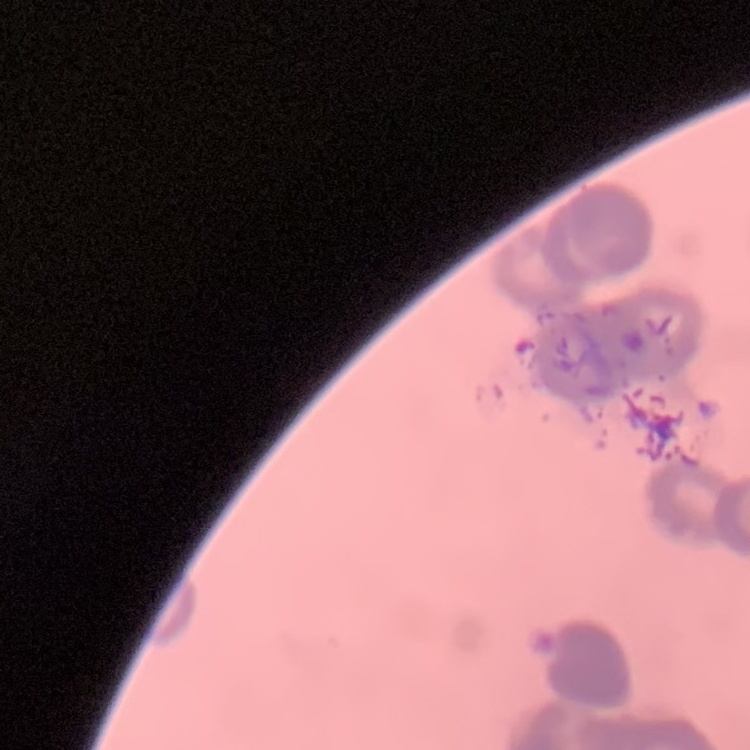

Summary:
  - Erythrocyte morphology: rouleaux formation
  - Preparation: thin peripheral smear
  - Stain: Field's or Giemsa
  - Image type: square crop of a larger photomicrograph